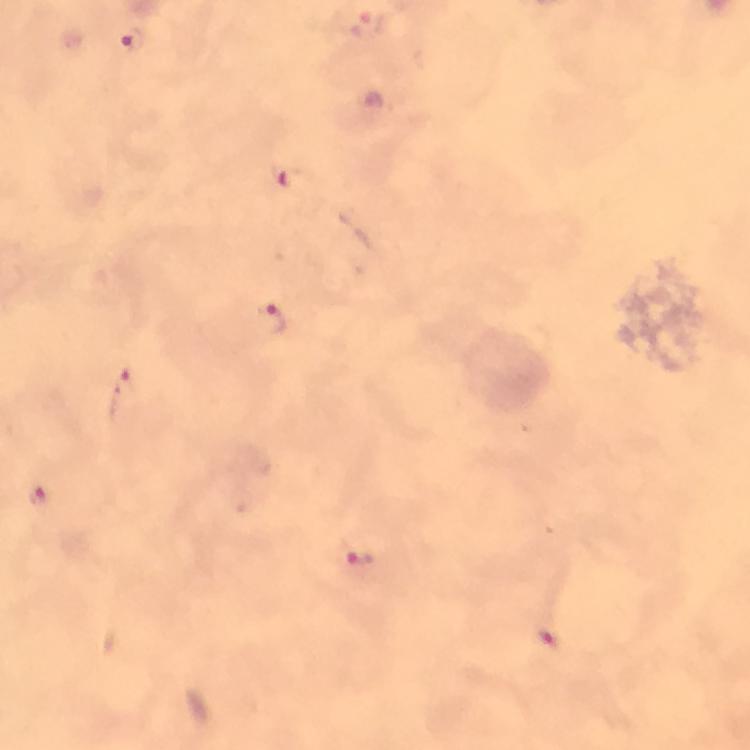

Approximate object centers, in pixels from the top-left corner. Malaria parasite locations: (x=132, y=40), (x=285, y=175), (x=273, y=318), (x=125, y=394), (x=39, y=495), (x=359, y=555), (x=547, y=638). Thick smear. Photographed through the microscope with a smartphone camera. Immersion oil was used. Image is 750×750 pixels. Giemsa stain. Cropped region of a single field of view. From a diagnostic examination for malaria. At 100x magnification.